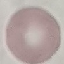
result = negative for malaria parasites
stain = Giemsa
preparation = thin smear
capture = smartphone camera at the microscope eyepiece
image type = cell patch, automatically extracted from a larger field of view and resized to 64 × 64 pixels